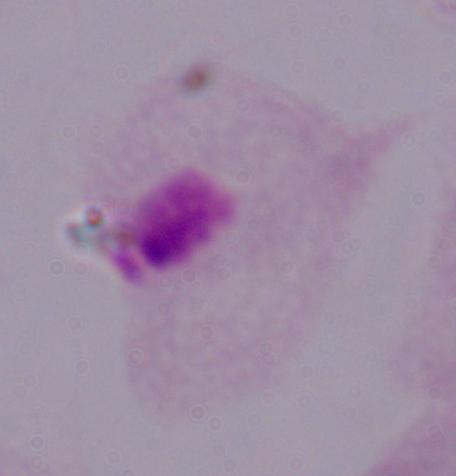
Summary:
  - Magnification: 1000x
  - Identification: trichomonad
  - Modality: micrograph